Assess the morphology of the erythrocytes.
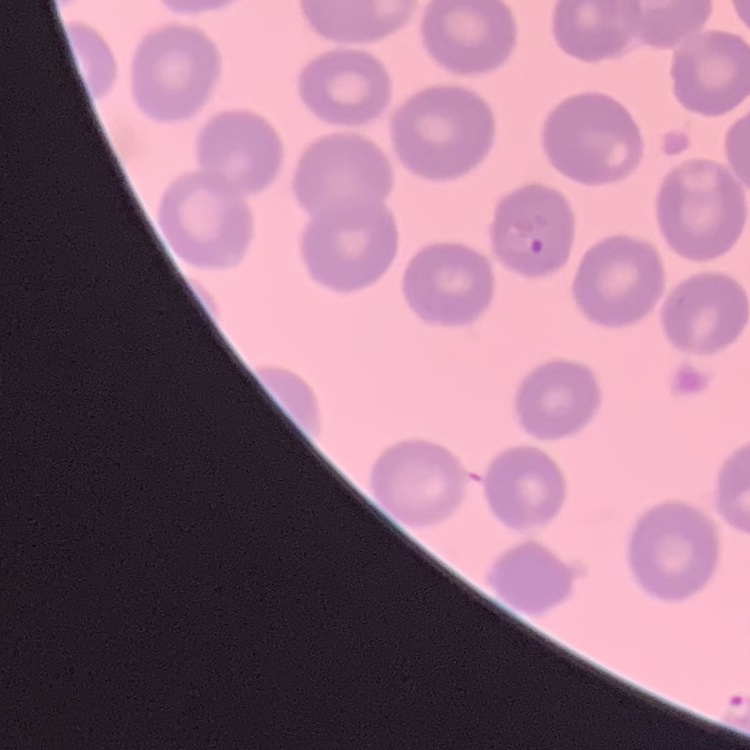

No rouleaux formation.

Summary:
  - Stain: Field's or Giemsa
  - Image type: one tile cut from a larger photomicrograph
  - Preparation: thin blood smear